Assess this cell for malaria.
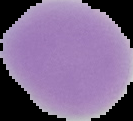
Uninfected.

{
  "image_type": "cell region segmented out of the field of view; surrounding area masked to black",
  "preparation": "thin blood smear",
  "image_size": "133×121 pixels"
}